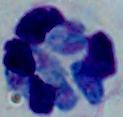
Summary:
  - Identification: white blood cell
  - Magnification: 1000x
  - Modality: photomicrograph